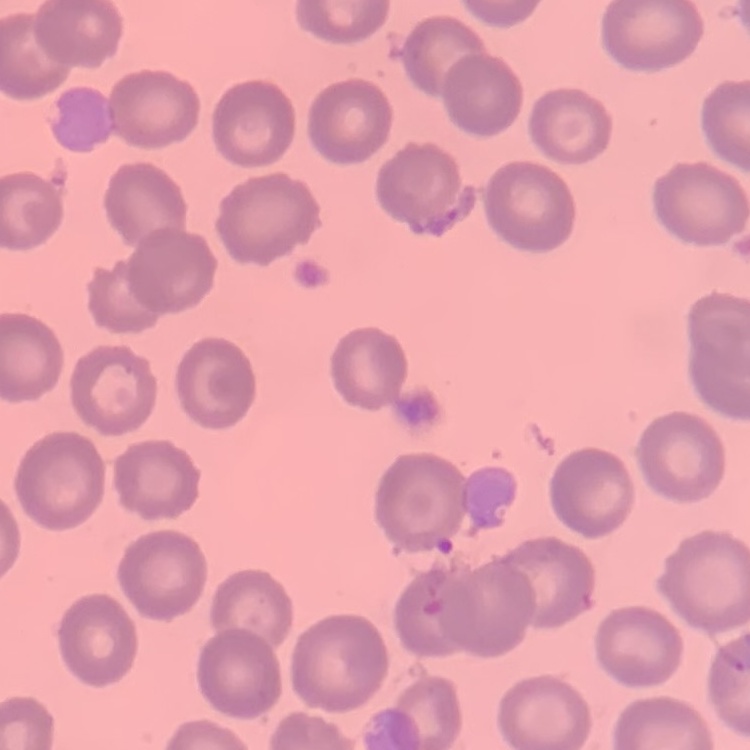
The red blood cells exhibit no rouleaux formation. Field's or Giemsa stain. Thin blood smear. One tile cut from a larger photomicrograph.